Assess the morphology of the erythrocytes.
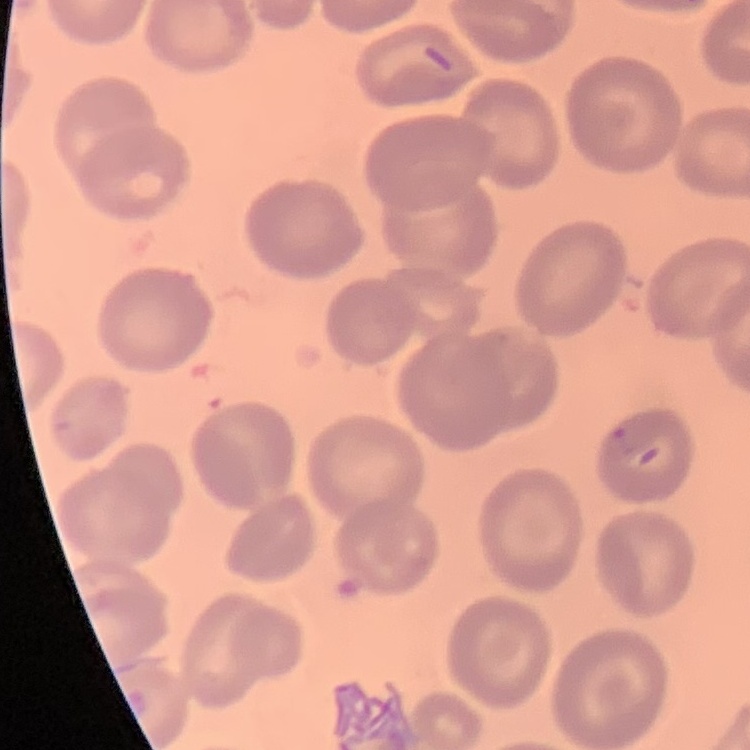

They show no rouleaux formation.

{
  "image_type": "one tile cut from a larger photomicrograph",
  "preparation": "thin blood film",
  "stain": "Field's or Giemsa"
}